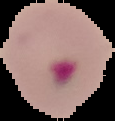 Image is 115×121 pixels. Segmented cell region on a black background. From a thin blood film. Result: Plasmodium parasites identified.